Classify this cell by malaria status.
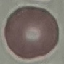
It is uninfected.

Summary:
  - Preparation: thin smear
  - Capture: smartphone through the microscope eyepiece
  - Stain: Giemsa
  - Image type: automatically extracted cell patch, resized to 64 × 64 pixels